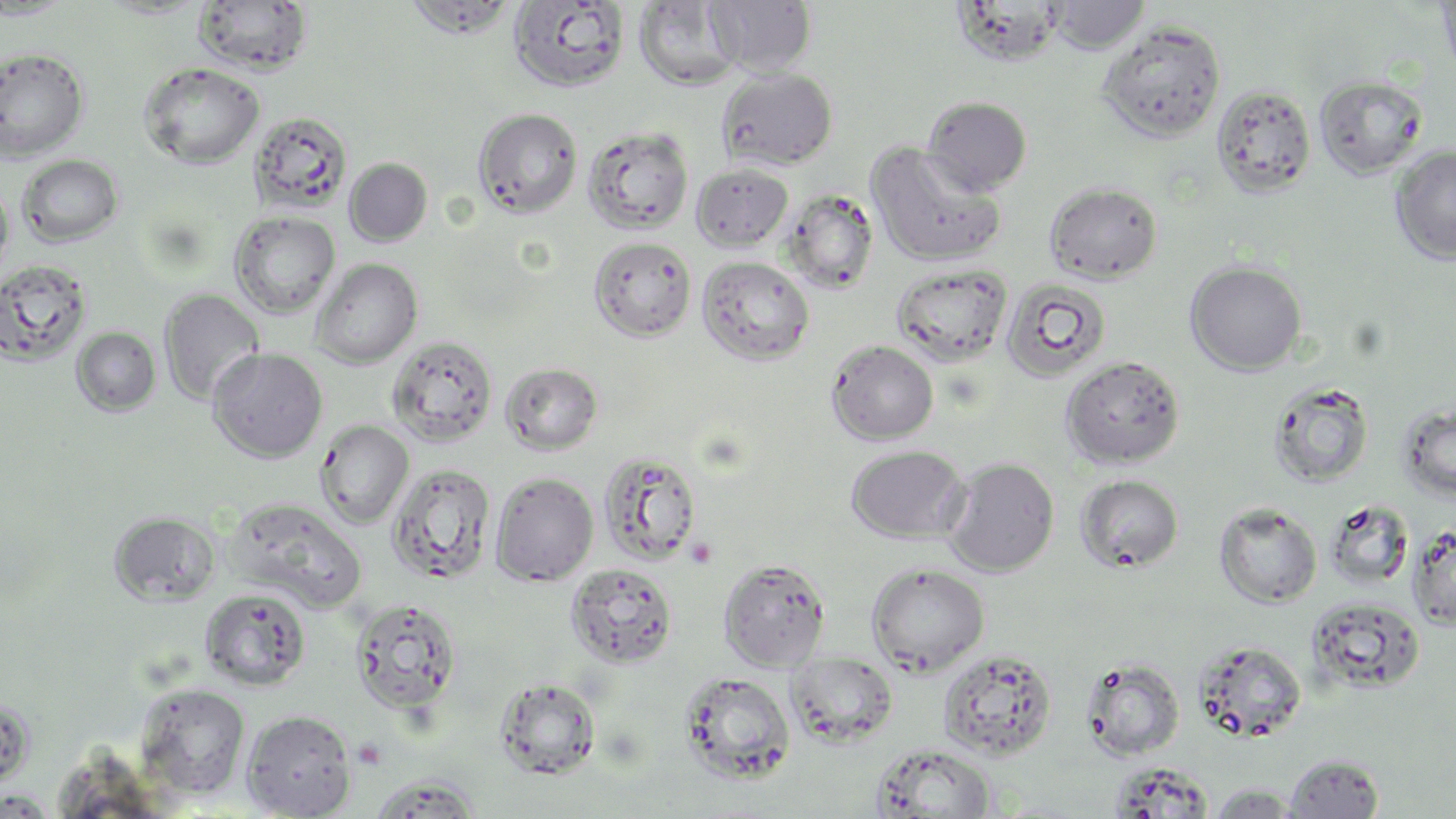

{
  "slide_level_diagnosis": "no evidence of blood parasites",
  "image_size": "1456×819 pixels",
  "preparation": "thin blood film",
  "modality": "optical microscopy",
  "field_of_view": "single",
  "stain": "May-Grünwald-Giemsa",
  "uninfected_red_blood_cell_locations": "approximate bounding boxes as [x1, y1, x2, y2] in pixels: [0, 0, 75, 20], [405, 0, 520, 39], [707, 0, 817, 76], [1435, 0, 1456, 82], [192, 1, 314, 76], [509, 1, 631, 93], [633, 1, 743, 91], [1047, 1, 1150, 53], [1096, 21, 1227, 143], [0, 46, 90, 162], [139, 62, 265, 169], [717, 67, 838, 170], [1314, 75, 1428, 179], [1210, 83, 1317, 198], [922, 96, 1032, 196], [473, 108, 582, 218], [248, 110, 353, 214], [582, 126, 694, 235], [866, 143, 1006, 267], [1390, 145, 1456, 265], [16, 154, 124, 247], [344, 158, 432, 246], [691, 163, 794, 252], [0, 181, 15, 283], [1044, 181, 1163, 283], [781, 189, 880, 294], [229, 211, 340, 318], [588, 236, 697, 342], [696, 255, 815, 366], [311, 258, 422, 368], [0, 259, 94, 366], [1185, 261, 1307, 375], [891, 262, 1014, 367], [1000, 276, 1113, 383], [159, 289, 265, 406], [71, 327, 161, 416], [387, 335, 498, 447], [826, 340, 939, 445], [208, 348, 328, 463], [1060, 356, 1186, 469], [500, 362, 603, 455], [1267, 380, 1374, 488], [1397, 401, 1456, 503], [315, 420, 414, 529], [846, 445, 968, 543], [598, 450, 703, 566], [942, 457, 1060, 577], [386, 463, 496, 585], [490, 471, 598, 586], [1075, 474, 1184, 573], [226, 498, 367, 610], [1324, 499, 1415, 592], [1213, 503, 1322, 608], [109, 511, 221, 606], [1406, 524, 1456, 630], [718, 558, 831, 671], [565, 563, 678, 668], [866, 563, 990, 676], [199, 588, 312, 691], [1306, 596, 1426, 694], [350, 598, 462, 717], [1192, 639, 1308, 743], [938, 648, 1057, 760], [787, 652, 898, 748], [1081, 657, 1185, 761], [678, 671, 796, 784], [494, 678, 601, 780], [134, 683, 251, 800], [241, 708, 357, 818], [872, 745, 996, 818], [1284, 753, 1385, 818], [366, 772, 484, 818], [1205, 784, 1306, 818], [0, 790, 57, 818]",
  "magnification": "1000x"
}